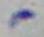
Summary:
  - Magnification: 1000x
  - Identification: Toxoplasma gondii
  - Modality: micrograph